Locate every uninfected red blood cell.
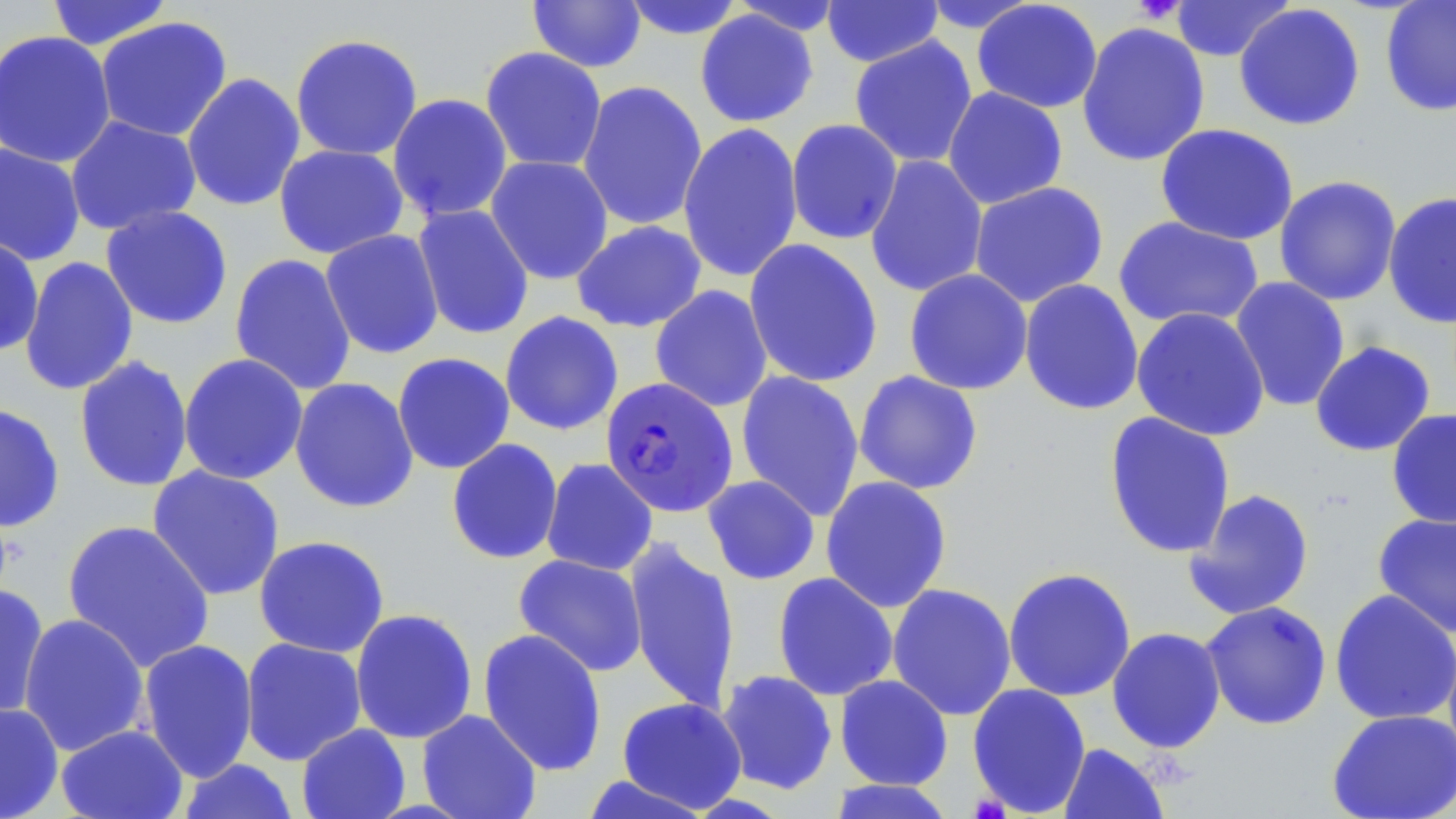
Approximate bounding boxes as named x1/y1/x2/y2 corners in pixels.
Uninfected red blood cells: (x1=45, y1=0, x2=175, y2=51), (x1=619, y1=0, x2=746, y2=40), (x1=821, y1=0, x2=943, y2=68), (x1=1168, y1=0, x2=1294, y2=62), (x1=527, y1=1, x2=647, y2=73), (x1=728, y1=1, x2=847, y2=36), (x1=916, y1=1, x2=1041, y2=35), (x1=971, y1=1, x2=1103, y2=114), (x1=1380, y1=1, x2=1456, y2=117), (x1=1234, y1=3, x2=1366, y2=131), (x1=695, y1=9, x2=819, y2=128), (x1=94, y1=16, x2=234, y2=142), (x1=1076, y1=21, x2=1210, y2=167), (x1=0, y1=29, x2=116, y2=168), (x1=289, y1=33, x2=424, y2=161), (x1=849, y1=35, x2=978, y2=168), (x1=479, y1=46, x2=607, y2=173), (x1=181, y1=72, x2=306, y2=212), (x1=577, y1=80, x2=708, y2=231), (x1=942, y1=87, x2=1068, y2=209), (x1=387, y1=93, x2=513, y2=222), (x1=64, y1=115, x2=202, y2=235), (x1=786, y1=119, x2=903, y2=245), (x1=678, y1=123, x2=803, y2=282), (x1=1155, y1=123, x2=1299, y2=246), (x1=0, y1=142, x2=86, y2=266), (x1=274, y1=144, x2=409, y2=259), (x1=865, y1=154, x2=988, y2=298), (x1=485, y1=155, x2=614, y2=285), (x1=1274, y1=175, x2=1402, y2=306), (x1=969, y1=181, x2=1109, y2=307), (x1=1383, y1=191, x2=1456, y2=329), (x1=412, y1=203, x2=534, y2=340), (x1=100, y1=205, x2=234, y2=329), (x1=1114, y1=216, x2=1265, y2=330), (x1=571, y1=220, x2=707, y2=333), (x1=320, y1=229, x2=444, y2=359), (x1=0, y1=236, x2=45, y2=356), (x1=743, y1=238, x2=883, y2=389), (x1=229, y1=253, x2=357, y2=395), (x1=19, y1=256, x2=139, y2=396), (x1=904, y1=268, x2=1033, y2=396), (x1=1229, y1=276, x2=1350, y2=412), (x1=1018, y1=278, x2=1144, y2=416), (x1=650, y1=285, x2=773, y2=412), (x1=1131, y1=307, x2=1270, y2=441), (x1=499, y1=311, x2=624, y2=436), (x1=1310, y1=340, x2=1436, y2=457), (x1=178, y1=352, x2=309, y2=485), (x1=392, y1=352, x2=515, y2=474), (x1=74, y1=355, x2=194, y2=493), (x1=735, y1=370, x2=865, y2=521), (x1=853, y1=370, x2=984, y2=495), (x1=289, y1=377, x2=419, y2=513), (x1=0, y1=402, x2=66, y2=533), (x1=1386, y1=408, x2=1456, y2=528), (x1=1103, y1=411, x2=1236, y2=559), (x1=446, y1=438, x2=563, y2=564), (x1=541, y1=457, x2=658, y2=576), (x1=147, y1=464, x2=285, y2=601), (x1=702, y1=475, x2=820, y2=585), (x1=820, y1=475, x2=952, y2=613), (x1=1183, y1=487, x2=1315, y2=621), (x1=1372, y1=511, x2=1456, y2=638), (x1=61, y1=519, x2=215, y2=672), (x1=253, y1=535, x2=390, y2=658), (x1=625, y1=536, x2=741, y2=716), (x1=513, y1=553, x2=648, y2=677), (x1=1003, y1=566, x2=1137, y2=702), (x1=772, y1=572, x2=898, y2=701), (x1=887, y1=582, x2=1017, y2=721), (x1=0, y1=583, x2=50, y2=721), (x1=1329, y1=589, x2=1456, y2=726), (x1=1200, y1=600, x2=1332, y2=730), (x1=349, y1=608, x2=478, y2=744), (x1=18, y1=613, x2=151, y2=756), (x1=1106, y1=626, x2=1226, y2=753), (x1=477, y1=628, x2=608, y2=776), (x1=240, y1=637, x2=367, y2=765), (x1=137, y1=638, x2=258, y2=783), (x1=716, y1=670, x2=838, y2=795), (x1=834, y1=674, x2=954, y2=790), (x1=967, y1=683, x2=1091, y2=817), (x1=617, y1=696, x2=747, y2=813), (x1=0, y1=701, x2=64, y2=819), (x1=1326, y1=708, x2=1456, y2=818), (x1=416, y1=709, x2=542, y2=819), (x1=296, y1=723, x2=410, y2=819), (x1=55, y1=724, x2=189, y2=819), (x1=1057, y1=742, x2=1170, y2=819), (x1=177, y1=758, x2=300, y2=819), (x1=580, y1=774, x2=715, y2=818), (x1=828, y1=779, x2=957, y2=819).

Platelet locations: (x1=1131, y1=1, x2=1188, y2=24). Plasmodium falciparum-infected red blood cell locations: (x1=600, y1=376, x2=738, y2=517). Slide-level diagnosis: Plasmodium falciparum. One field of a larger specimen. 1000x magnification. Light microscopy. Thin blood smear. May-Grünwald-Giemsa-stained preparation. Image is 1456×819 pixels.